Name the blood parasite species.
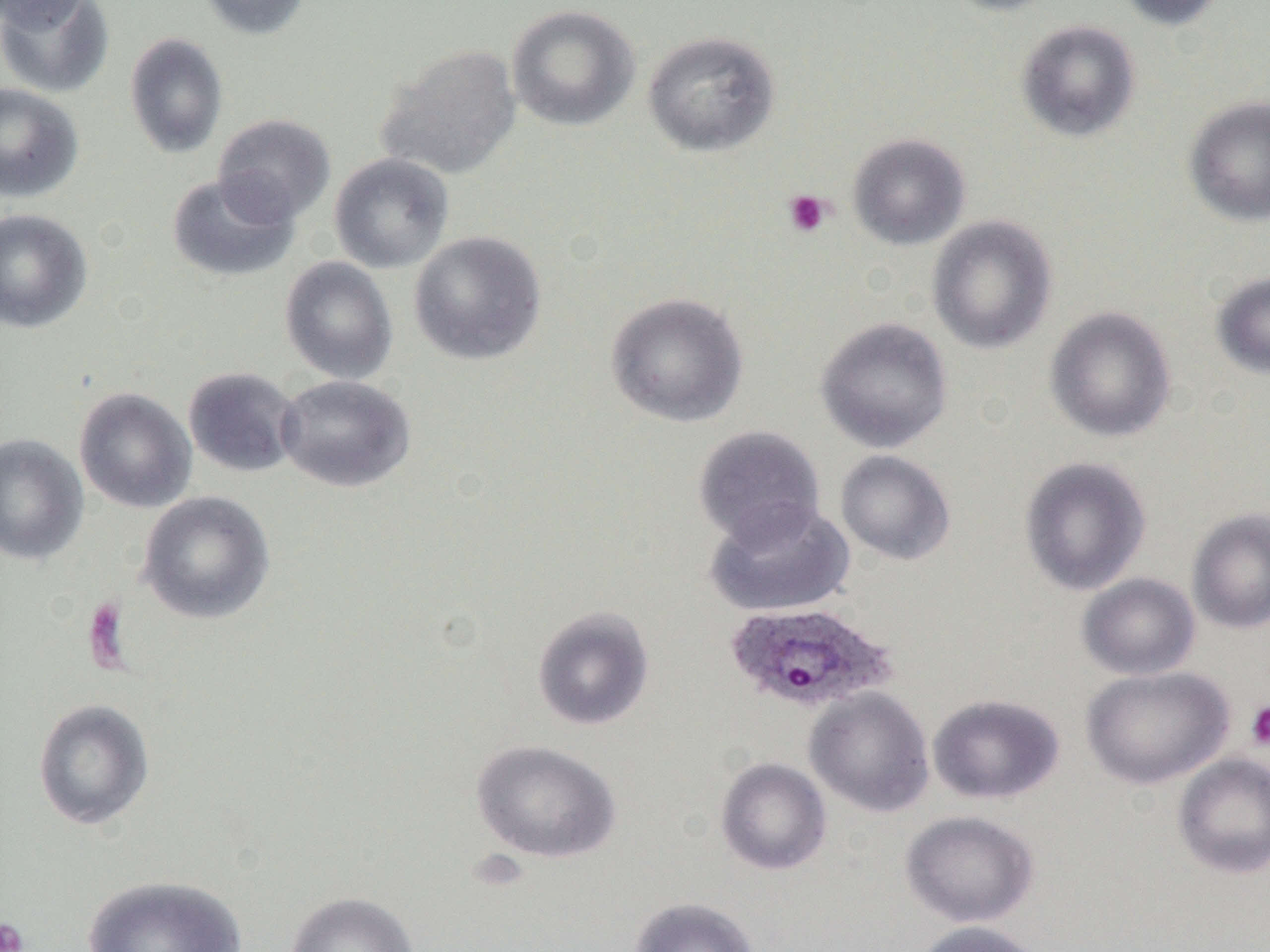

Plasmodium ovale.

Approximate bounding boxes as (x1, y1, x2, y2) in pixels. Plasmodium ovale-infected red blood cell locations: (723, 601, 897, 715). Uninfected red blood cell locations: (0, 0, 115, 99), (197, 0, 311, 40), (938, 0, 1068, 16), (1112, 0, 1231, 31), (0, 1, 91, 31), (506, 4, 640, 132), (1015, 19, 1141, 143), (642, 29, 780, 157), (124, 32, 228, 159), (376, 44, 522, 180), (0, 82, 84, 203), (1184, 95, 1270, 227), (213, 113, 336, 225), (847, 132, 970, 250), (328, 153, 455, 274), (166, 172, 300, 283), (0, 208, 93, 333), (926, 214, 1057, 354), (408, 230, 547, 365), (279, 256, 398, 384), (1211, 271, 1270, 379), (605, 292, 749, 428), (1044, 306, 1176, 442), (815, 316, 953, 453), (182, 366, 302, 478), (275, 374, 415, 492), (73, 387, 197, 513), (692, 425, 826, 548), (0, 434, 88, 565), (835, 449, 956, 566), (1019, 457, 1152, 595), (137, 491, 277, 624), (705, 501, 854, 618), (1187, 508, 1270, 635), (1077, 573, 1201, 680), (531, 606, 655, 731), (1080, 665, 1234, 790), (803, 686, 935, 817), (928, 693, 1064, 805), (33, 698, 155, 831), (470, 739, 621, 864), (1171, 752, 1270, 879), (715, 757, 832, 876), (900, 810, 1040, 928), (81, 874, 248, 951), (283, 891, 421, 952), (629, 896, 760, 952), (912, 920, 1048, 952). Platelet locations: (784, 189, 832, 237), (1244, 701, 1270, 751), (0, 917, 30, 952). Single field of view. Thin blood film. Image is 1270×952 pixels. Captured at 1000x magnification. Light microscopy.